Describe the morphology of the erythrocytes.
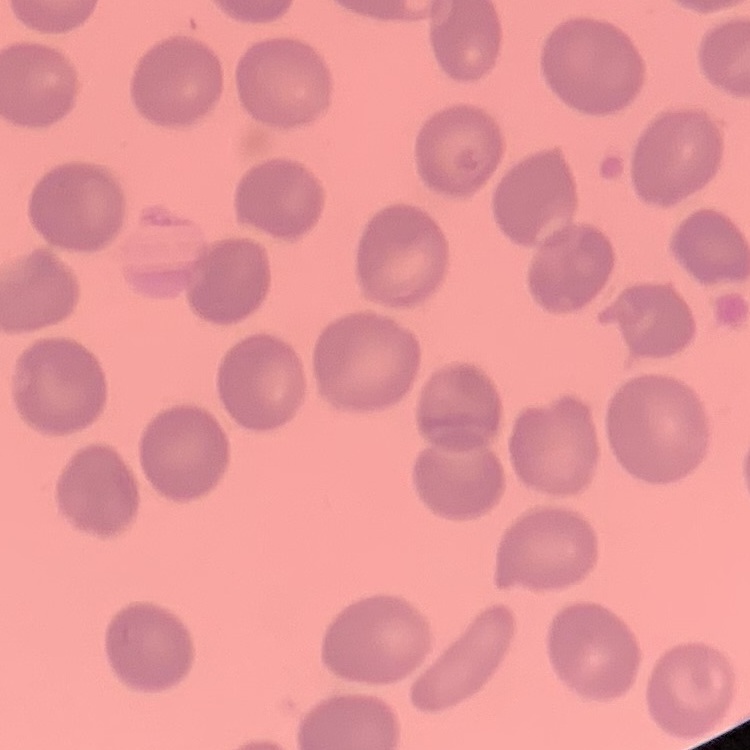
No rouleaux formation.

Thin blood smear. Field's or Giemsa stain. One tile cut from a larger photomicrograph.